Identify the parasite.
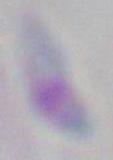
This is Toxoplasma gondii.

Photomicrograph. Captured at 1000x magnification.